Locate and identify every blood parasite.
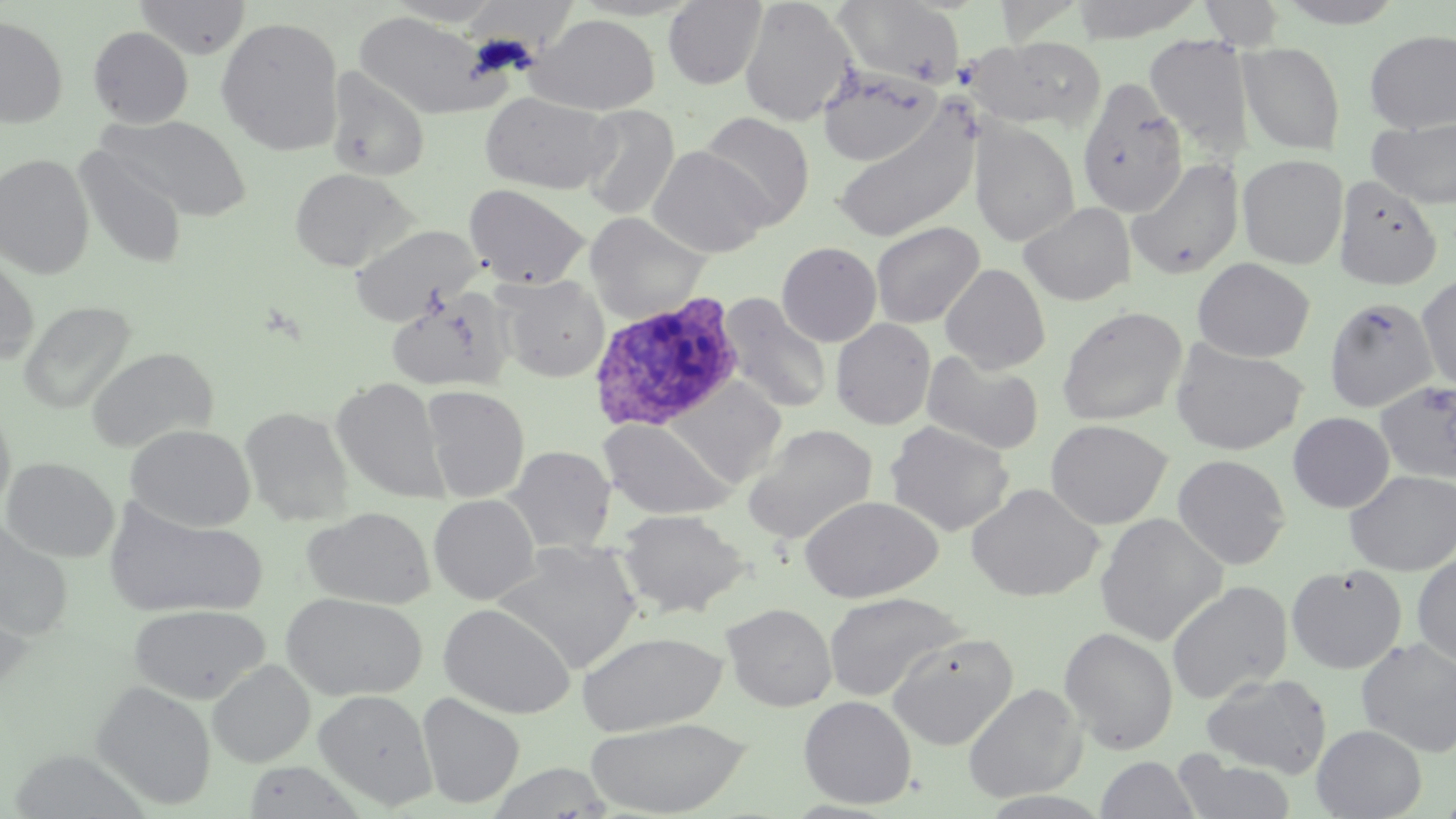

Approximate bounding boxes as (x1, y1, x2, y2) in pixels.
Plasmodium ovale-infected red blood cells: (589, 292, 744, 431).
No Plasmodium falciparum, Plasmodium malariae, Plasmodium vivax, Babesia divergens, or Trypanosoma brucei observed.

Uninfected red blood cell locations: (135, 0, 251, 59), (663, 0, 767, 89), (739, 0, 855, 126), (833, 0, 965, 88), (1065, 0, 1209, 43), (1200, 0, 1286, 50), (386, 1, 504, 26), (1273, 1, 1407, 28), (354, 11, 498, 118), (529, 14, 660, 115), (0, 15, 68, 128), (215, 17, 345, 155), (88, 26, 193, 128), (1364, 29, 1456, 133), (1144, 34, 1254, 155), (964, 37, 1108, 133), (1239, 41, 1346, 155), (818, 66, 941, 168), (325, 68, 430, 182), (1077, 76, 1187, 218), (479, 91, 617, 194), (579, 105, 679, 221), (832, 105, 980, 244), (699, 111, 816, 228), (100, 114, 251, 221), (1366, 117, 1456, 209), (969, 121, 1080, 246), (648, 146, 772, 258), (75, 147, 186, 268), (0, 153, 94, 279), (1237, 154, 1348, 269), (1126, 158, 1245, 281), (290, 168, 415, 272), (1332, 175, 1443, 291), (464, 185, 588, 289), (1018, 202, 1136, 306), (585, 212, 710, 324), (870, 221, 985, 329), (349, 224, 480, 325), (777, 242, 882, 347), (0, 250, 39, 368), (1192, 258, 1315, 362), (940, 263, 1051, 373), (1417, 273, 1456, 392), (496, 276, 609, 382), (384, 288, 514, 392), (719, 294, 833, 415), (1324, 297, 1439, 413), (19, 300, 136, 414), (1056, 305, 1188, 426), (831, 318, 935, 430), (1170, 339, 1309, 455), (86, 347, 218, 452), (922, 351, 1044, 455), (332, 377, 449, 504), (662, 378, 788, 486), (1375, 380, 1456, 482), (421, 385, 530, 502), (0, 402, 16, 520), (239, 407, 354, 526), (1288, 412, 1395, 512), (598, 418, 736, 520), (1045, 419, 1172, 529), (885, 420, 1015, 536), (743, 423, 878, 544), (126, 424, 255, 532), (504, 445, 616, 553), (1172, 454, 1291, 570), (2, 457, 119, 562), (1343, 469, 1456, 576), (966, 482, 1104, 601), (428, 494, 540, 604), (799, 495, 942, 603), (104, 501, 268, 619), (302, 507, 435, 609), (617, 509, 751, 618), (1095, 513, 1228, 645), (0, 520, 73, 641), (493, 540, 642, 673), (1412, 553, 1456, 668), (1286, 564, 1408, 674), (1167, 580, 1293, 704), (823, 591, 966, 702), (281, 592, 429, 701), (0, 596, 34, 701), (438, 603, 575, 719), (721, 603, 838, 711), (129, 604, 269, 702), (1059, 626, 1178, 754), (576, 631, 726, 737), (887, 633, 1019, 750), (1355, 638, 1456, 757), (207, 660, 314, 767), (1201, 672, 1332, 778), (92, 680, 217, 810), (963, 683, 1086, 802), (313, 689, 438, 809), (417, 692, 525, 809), (798, 695, 917, 809), (585, 717, 751, 817), (1312, 725, 1427, 818), (1173, 755, 1297, 819), (1096, 756, 1199, 818), (242, 760, 366, 819), (485, 763, 616, 818), (977, 790, 1112, 818). Slide-level diagnosis: Plasmodium ovale. May-Grünwald-Giemsa stain. Image is 1456×819 pixels. Thin blood film. Optical microscopy. One field of a larger specimen. Captured at 1000x magnification.